Identify the preparation type.
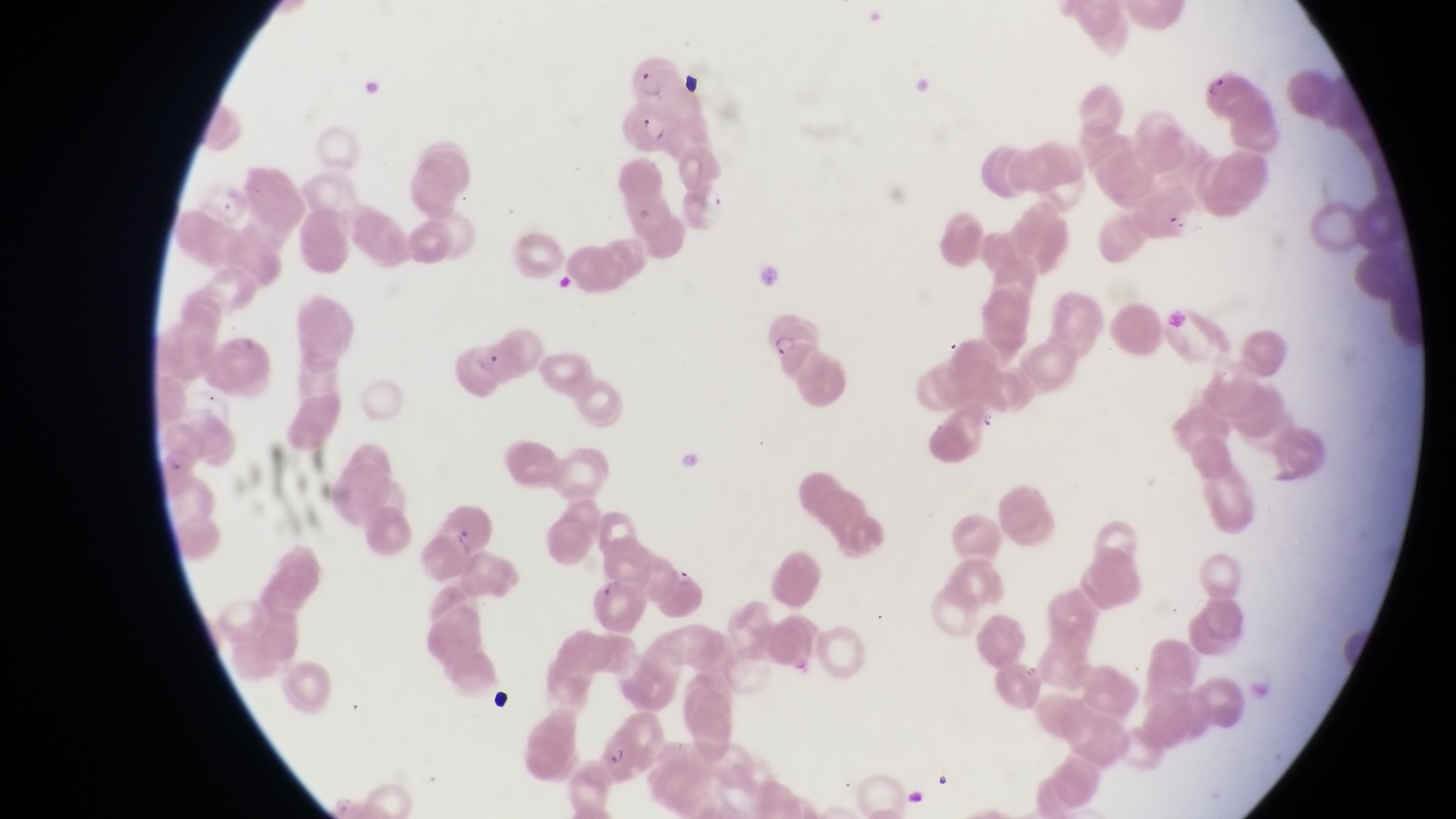

This is a thin smear.

Approximate bounding boxes as left top right bottom in pixels.
Summary:
  - Trophozoite locations: 695 180 729 217; 975 409 998 435; 673 566 697 590
  - Artifact (platelet-like body, stain precipitate, or debris) locations: 683 71 705 98; 485 684 515 715
  - Parasitised red blood cell locations: 1207 72 1256 118; 621 100 676 156; 756 309 815 364; 452 343 511 401; 592 576 644 632; 582 704 658 780
  - Image size: 1456×819 pixels
  - Field of view: single
  - Magnification: 1000x
  - Capture: smartphone photograph through the eyepiece of an Olympus CX-23 microscope
  - Country: Uganda